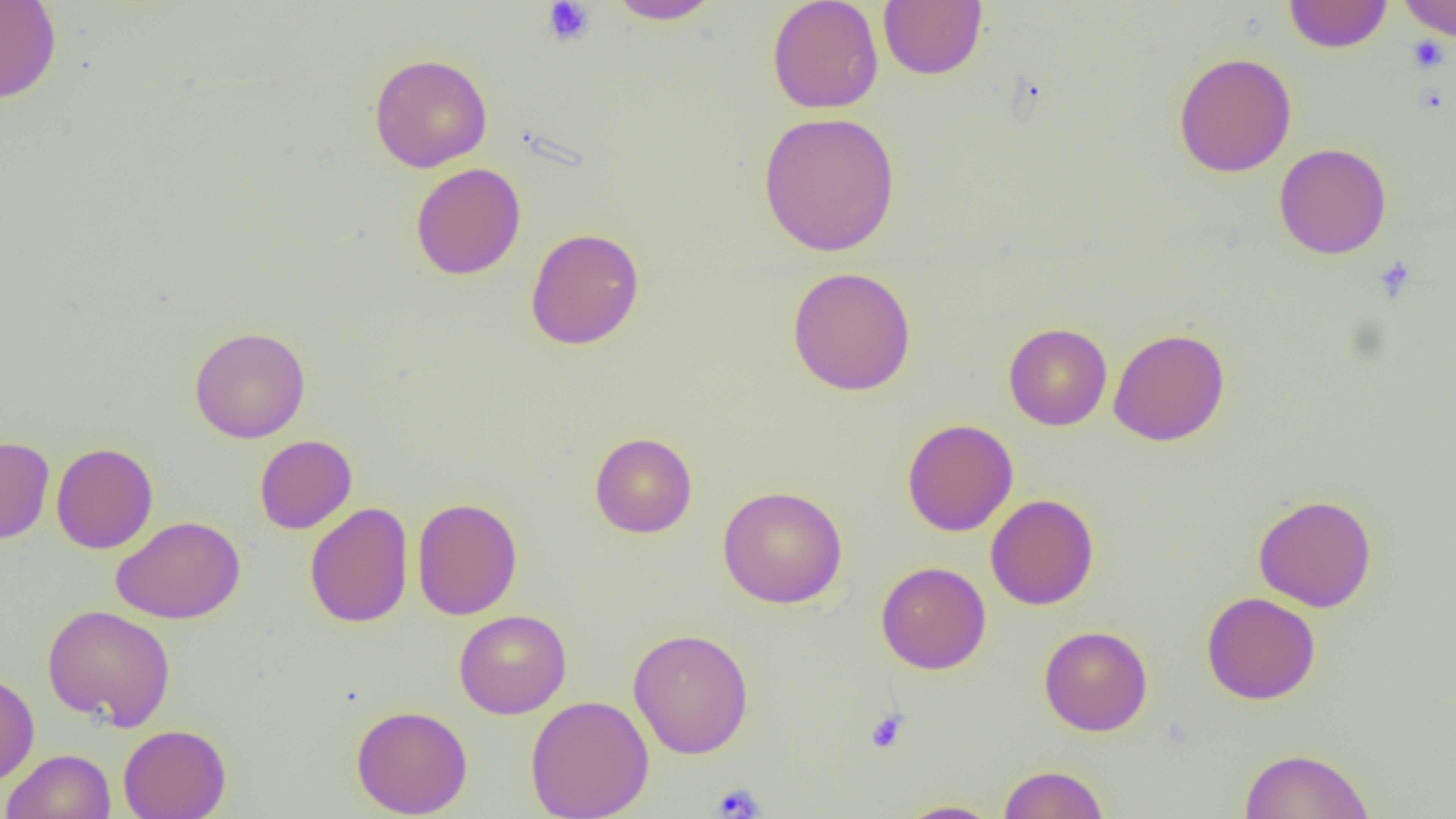
Summary:
  - Coordinate format: approximate bounding boxes as named x1/y1/x2/y2 corners in pixels
  - Uninfected red blood cell locations: (x1=605, y1=0, x2=722, y2=24), (x1=767, y1=0, x2=884, y2=114), (x1=1283, y1=0, x2=1393, y2=53), (x1=1398, y1=0, x2=1456, y2=41), (x1=0, y1=1, x2=62, y2=103), (x1=878, y1=1, x2=987, y2=80), (x1=369, y1=53, x2=493, y2=172), (x1=1173, y1=53, x2=1297, y2=177), (x1=757, y1=111, x2=901, y2=257), (x1=1274, y1=142, x2=1392, y2=260), (x1=411, y1=162, x2=526, y2=280), (x1=525, y1=227, x2=644, y2=350), (x1=787, y1=266, x2=916, y2=396), (x1=1003, y1=323, x2=1112, y2=431), (x1=189, y1=326, x2=310, y2=443), (x1=1108, y1=328, x2=1229, y2=446), (x1=902, y1=419, x2=1018, y2=536), (x1=589, y1=432, x2=697, y2=538), (x1=254, y1=435, x2=356, y2=534), (x1=0, y1=436, x2=55, y2=544), (x1=51, y1=442, x2=158, y2=554), (x1=718, y1=485, x2=848, y2=609), (x1=985, y1=493, x2=1099, y2=610), (x1=1253, y1=494, x2=1377, y2=612), (x1=411, y1=497, x2=522, y2=620), (x1=304, y1=502, x2=413, y2=628), (x1=112, y1=515, x2=245, y2=624), (x1=876, y1=561, x2=991, y2=674), (x1=1201, y1=591, x2=1321, y2=704), (x1=41, y1=604, x2=176, y2=730), (x1=454, y1=609, x2=572, y2=718), (x1=1039, y1=625, x2=1152, y2=736), (x1=628, y1=628, x2=754, y2=759), (x1=0, y1=672, x2=39, y2=785), (x1=525, y1=694, x2=654, y2=819), (x1=351, y1=704, x2=473, y2=818), (x1=118, y1=724, x2=231, y2=819), (x1=1238, y1=747, x2=1375, y2=819), (x1=1, y1=749, x2=116, y2=819), (x1=998, y1=764, x2=1110, y2=819), (x1=896, y1=800, x2=1004, y2=818)
  - Platelet locations: (x1=541, y1=1, x2=595, y2=46), (x1=1408, y1=35, x2=1449, y2=73), (x1=1373, y1=256, x2=1418, y2=303), (x1=865, y1=709, x2=909, y2=753), (x1=711, y1=782, x2=765, y2=818)
  - Slide-level diagnosis: negative for blood parasites
  - Modality: optical microscopy
  - Field of view: one of a larger specimen
  - Image size: 1456×819 pixels
  - Magnification: 1000x
  - Preparation: thin blood film